Point out every Plasmodium parasite.
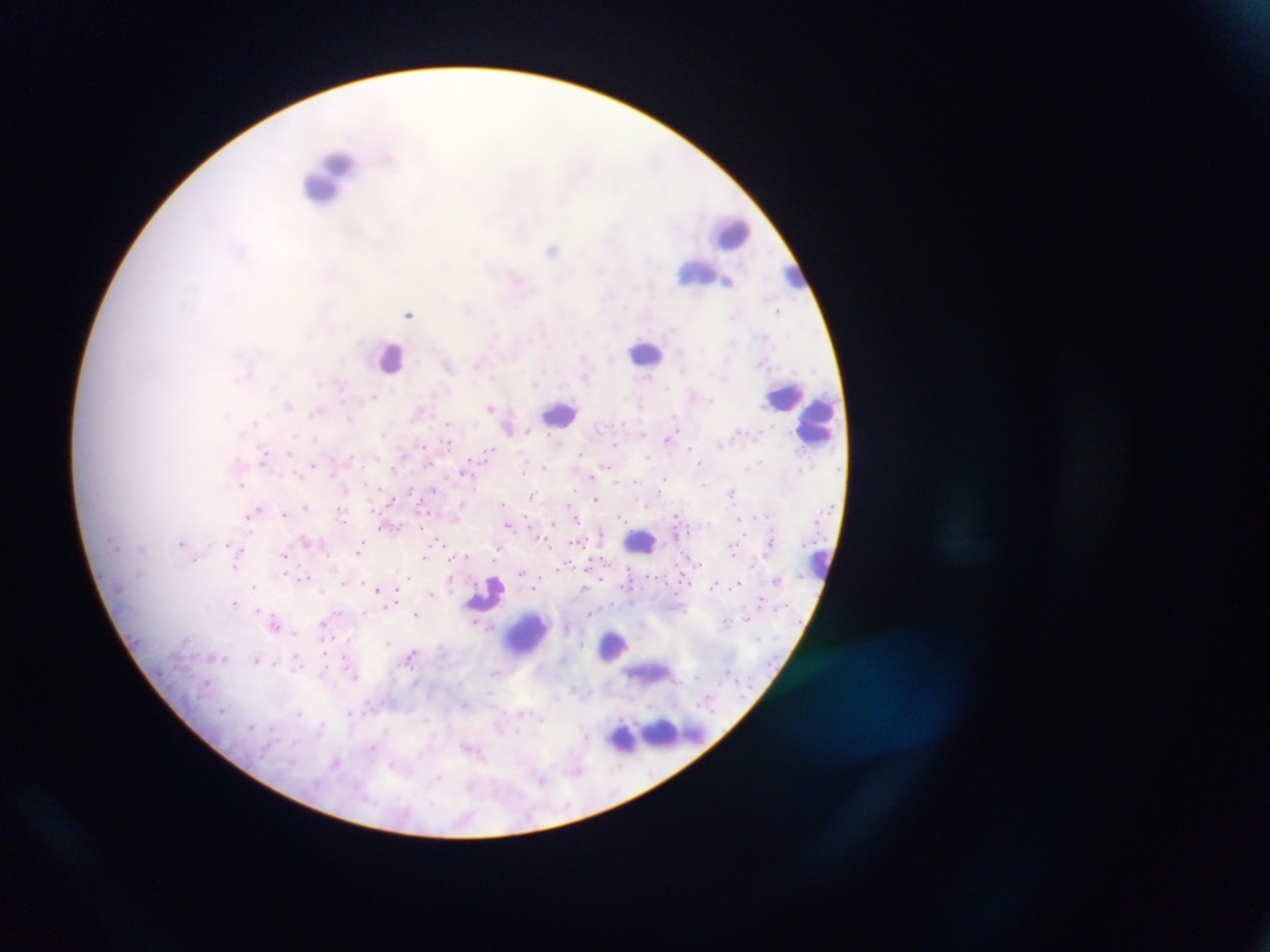

Approximate centers as [x, y] in pixels.
Plasmodium parasites: [521, 234], [553, 249], [601, 269], [728, 281], [468, 309], [777, 310], [409, 313], [610, 359], [477, 363], [682, 370], [586, 378], [648, 378], [375, 396], [289, 405], [491, 407], [419, 410], [316, 412], [674, 417], [350, 419], [255, 422], [448, 424], [529, 432], [383, 433], [644, 433], [553, 438], [667, 439], [449, 444], [615, 444], [691, 448], [488, 452], [289, 453], [580, 453], [263, 455], [352, 457], [648, 457], [761, 462], [699, 463], [314, 464], [429, 464], [606, 466], [755, 466], [544, 467], [747, 468], [524, 471], [464, 472], [299, 476], [665, 479], [635, 482], [241, 484], [704, 485], [434, 490], [731, 492], [532, 496], [596, 498], [391, 500], [502, 503], [306, 507], [258, 508], [340, 510], [253, 511], [285, 513], [676, 516], [621, 517], [577, 519], [553, 523], [508, 525], [383, 527], [602, 533], [545, 540], [438, 542], [576, 542], [181, 543], [228, 544], [359, 547], [141, 548], [498, 548], [732, 550], [285, 554], [424, 558], [194, 561], [698, 562], [752, 563], [562, 565], [236, 567], [522, 572], [284, 573], [408, 576], [306, 577], [345, 582], [738, 583], [715, 584], [254, 586], [535, 588], [378, 590], [431, 593], [396, 596], [760, 599], [235, 602], [391, 603], [257, 609], [590, 613], [415, 614], [747, 618], [276, 622], [726, 622], [323, 623], [475, 623], [294, 633], [388, 642], [411, 655], [224, 658], [296, 658], [256, 659], [275, 663], [494, 673], [490, 695], [465, 705], [223, 710], [299, 712], [349, 712], [541, 720], [252, 726], [320, 730], [517, 731], [587, 735], [293, 743], [372, 748], [467, 748], [335, 763], [394, 766], [578, 771], [436, 779], [541, 781].

Leukocyte locations (subset; some below the resolvable size): [328, 177], [730, 233], [697, 272], [791, 273], [646, 353], [390, 356], [785, 395], [560, 413], [819, 418], [641, 543], [818, 561], [484, 594], [527, 634], [614, 646], [648, 673], [673, 733], [625, 738]. Mobile-phone photograph taken through the microscope. Collected in Ghana. Image is 1270×952 pixels. Thick blood film. Single field of view.